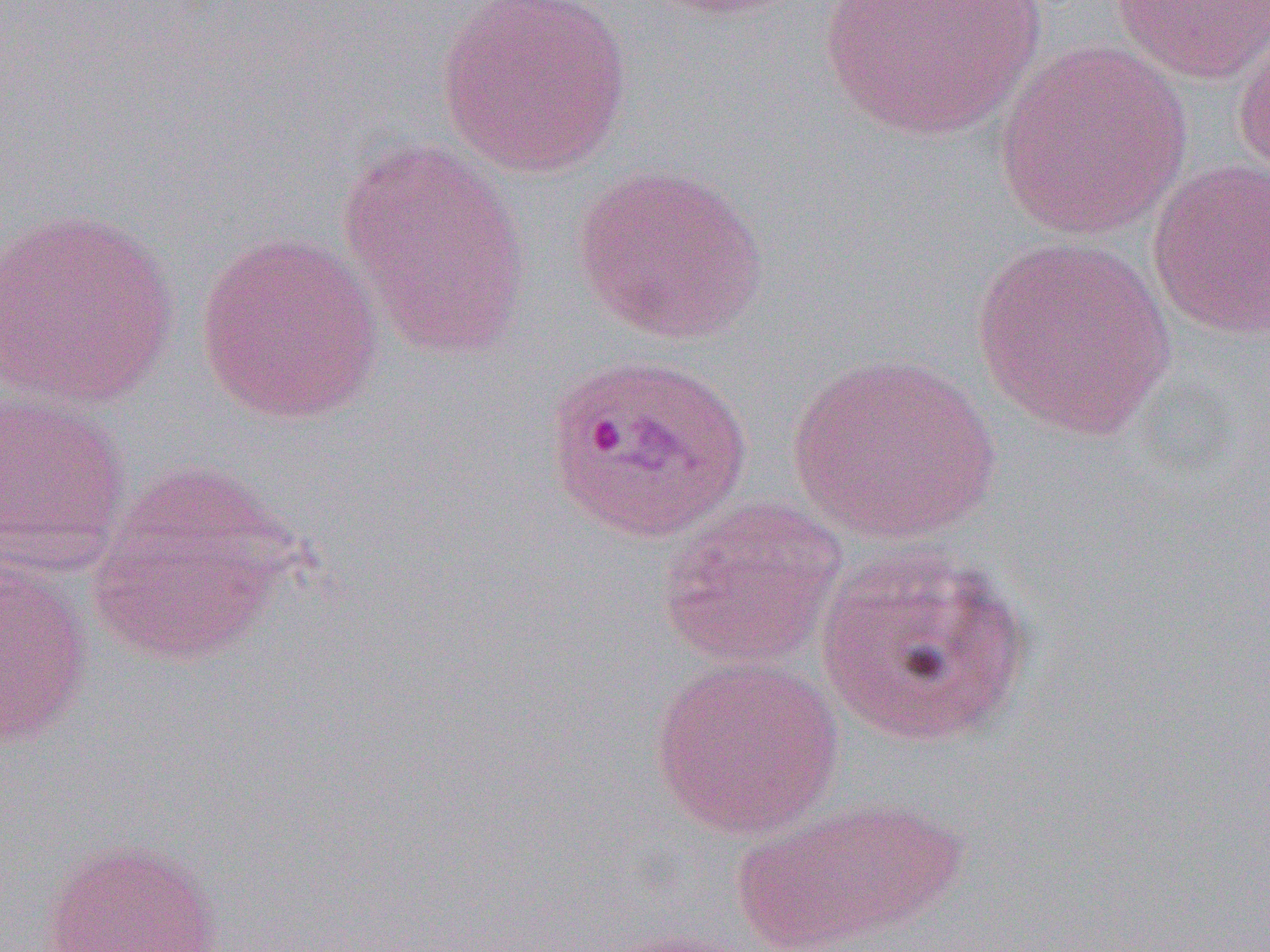
Approximate bounding boxes as (x1,y1)-(x2,y2) corner pairs in pixels. Plasmodium ovale-infected red blood cell locations: (543,352)-(752,545). Uninfected red blood cell locations: (816,0)-(1046,144), (1109,0)-(1269,86), (437,1)-(631,178), (1232,17)-(1270,188), (993,39)-(1193,242), (338,140)-(533,359), (1146,158)-(1270,339), (572,164)-(768,345), (0,206)-(180,411), (195,230)-(386,424), (970,236)-(1178,441), (786,352)-(1003,544), (0,390)-(133,573), (88,462)-(305,665), (656,496)-(848,670), (816,540)-(1032,747), (0,558)-(93,749), (649,655)-(842,839), (730,796)-(968,949), (42,836)-(223,951). Slide-level diagnosis: Plasmodium ovale. Image is 1270×952 pixels. Captured at 1000x magnification. Single field of view. Optical microscopy. Thin blood film.